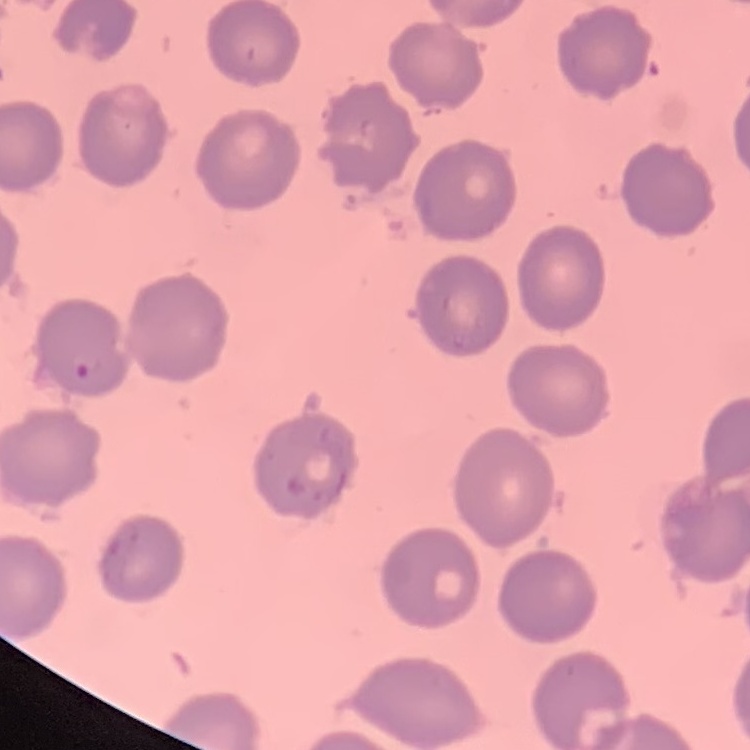
Summary:
  - Erythrocyte morphology: no rouleaux formation
  - Preparation: thin blood smear
  - Image type: square crop of a larger photomicrograph
  - Stain: Field's or Giemsa